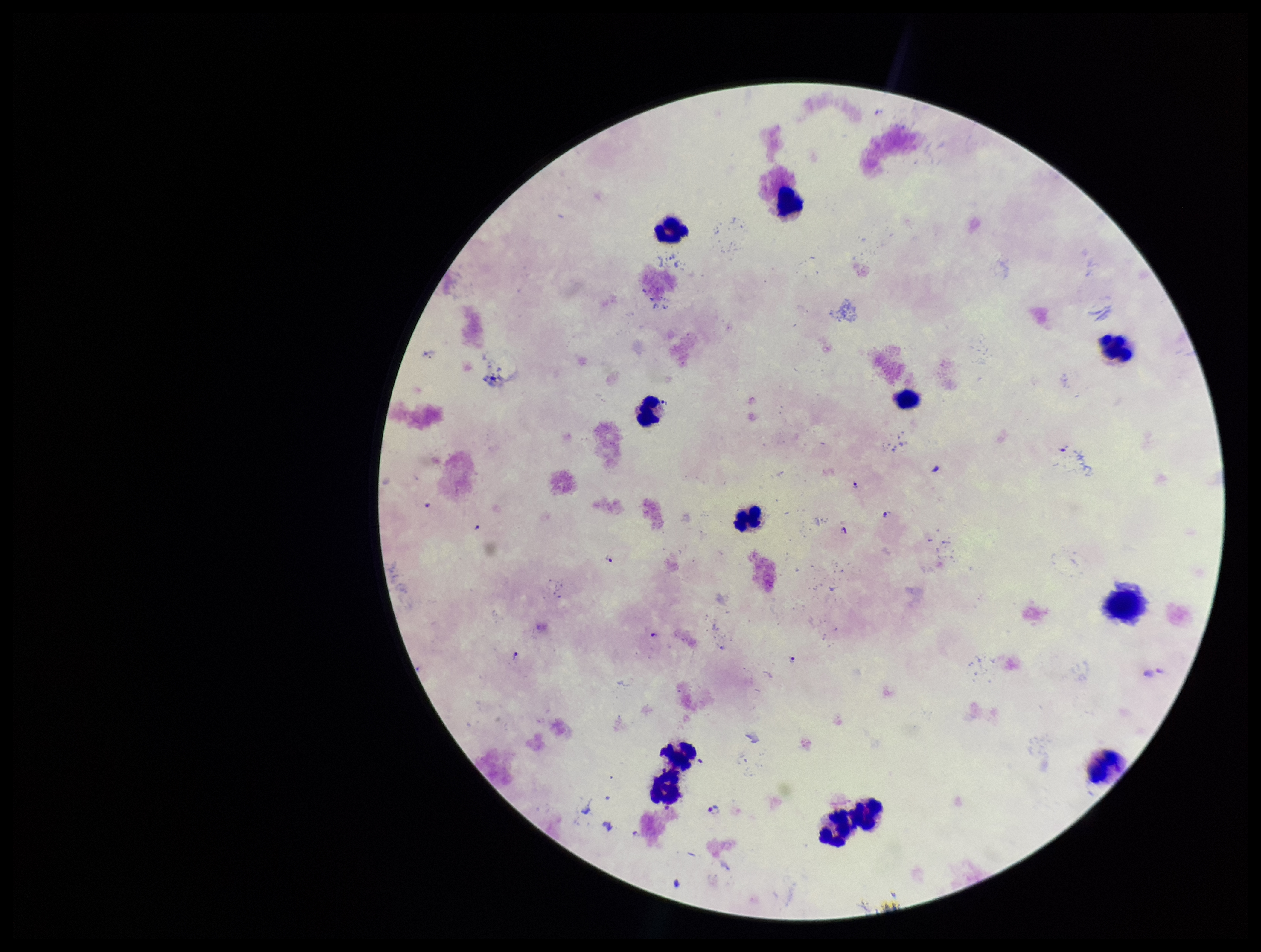
Summary:
  - Species reported for this patient: Plasmodium falciparum
  - Preparation: thick smear
  - Parasite count: 11
  - Plasmodium parasites: identified
  - Stain: Giemsa
  - Leukocyte count: 12
  - Patient malaria status: infected
  - Image size: 1261×952 pixels
  - Capture: smartphone photograph through the microscope eyepiece
  - Field of view: single